Identify the blood parasite species.
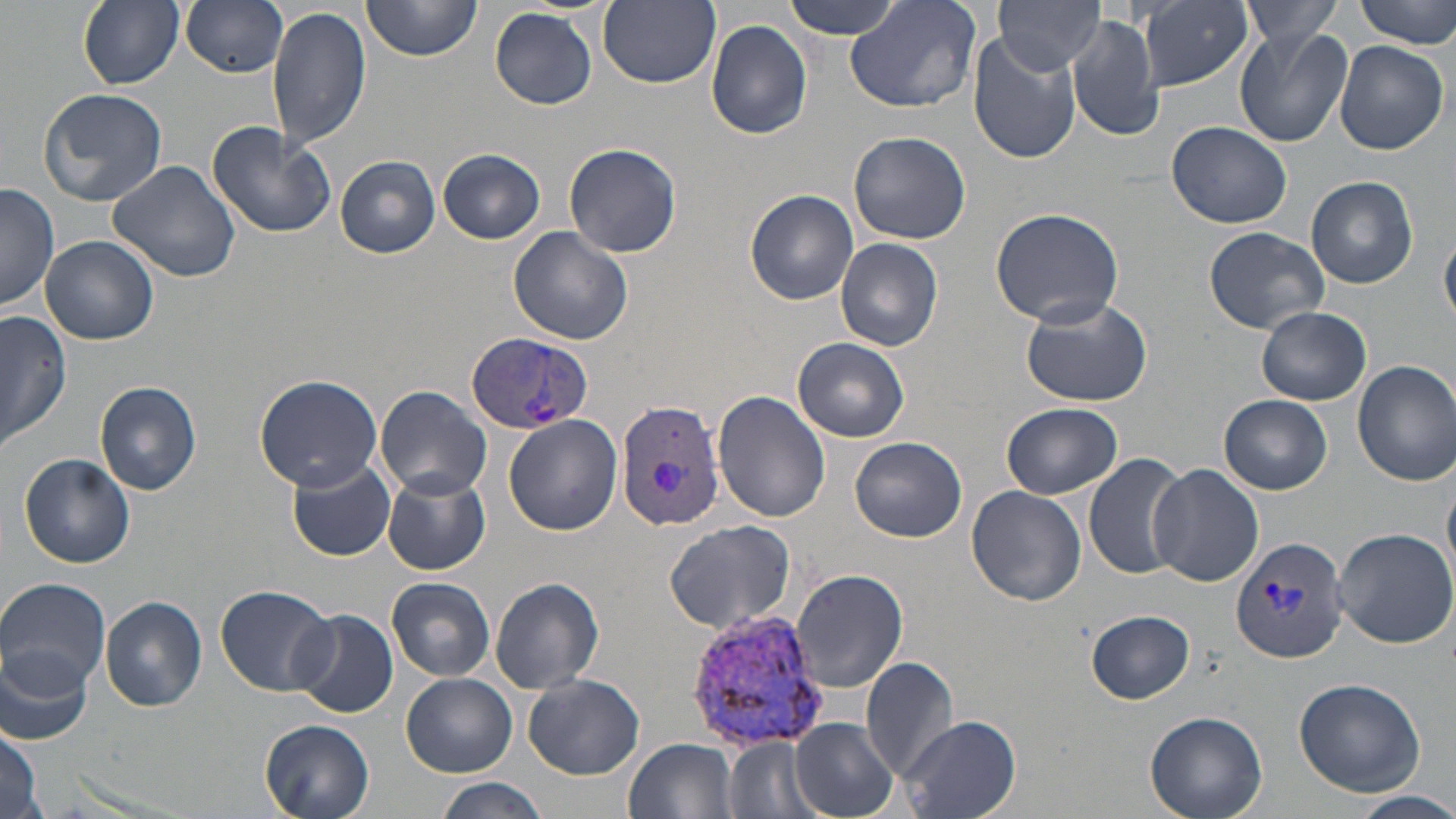

Plasmodium vivax.

Approximate bounding boxes as [x1, y1, x2, y2] in pixels. Plasmodium vivax-infected red blood cell locations: [466, 334, 594, 431], [615, 397, 727, 534], [1232, 538, 1351, 661], [682, 609, 832, 755]. Uninfected red blood cell locations: [78, 0, 184, 90], [181, 0, 290, 77], [361, 0, 480, 60], [783, 0, 907, 40], [844, 0, 982, 115], [1139, 0, 1252, 92], [1239, 0, 1344, 49], [1354, 0, 1456, 47], [599, 1, 720, 88], [992, 1, 1104, 73], [266, 5, 372, 149], [490, 7, 598, 109], [1068, 12, 1162, 140], [706, 20, 812, 140], [1234, 26, 1351, 147], [966, 33, 1082, 163], [1334, 39, 1448, 156], [37, 87, 168, 208], [206, 120, 337, 240], [1167, 122, 1295, 230], [848, 130, 970, 244], [563, 142, 683, 258], [439, 149, 544, 244], [336, 155, 440, 257], [107, 159, 240, 282], [1306, 176, 1418, 288], [1, 183, 59, 311], [75, 187, 226, 323], [746, 189, 859, 305], [989, 206, 1125, 327], [508, 227, 635, 348], [1203, 227, 1331, 334], [1441, 232, 1456, 327], [41, 236, 158, 345], [836, 237, 944, 352], [1018, 292, 1154, 406], [1256, 306, 1371, 406], [0, 310, 72, 454], [793, 339, 909, 441], [1353, 360, 1456, 485], [254, 373, 383, 491], [95, 381, 202, 494], [374, 385, 491, 500], [713, 390, 832, 523], [1219, 395, 1331, 494], [1001, 403, 1123, 500], [503, 414, 621, 536], [851, 437, 967, 542], [1083, 452, 1190, 583], [20, 453, 136, 568], [287, 457, 395, 561], [1148, 464, 1264, 587], [383, 472, 491, 575], [966, 485, 1087, 606], [666, 519, 797, 634], [1329, 526, 1456, 649], [790, 567, 908, 693], [387, 577, 496, 681], [490, 577, 604, 693], [0, 578, 111, 694], [215, 583, 337, 696], [99, 596, 207, 710], [1086, 610, 1196, 703], [291, 611, 398, 719], [1, 648, 95, 749], [861, 655, 960, 784], [403, 673, 516, 776], [523, 673, 644, 779], [1292, 678, 1425, 796], [1145, 711, 1267, 819], [900, 715, 1020, 819], [790, 718, 899, 819], [260, 719, 376, 819], [0, 729, 42, 819], [626, 736, 739, 819], [724, 736, 816, 819], [433, 777, 549, 819], [1343, 790, 1456, 819]. 1000x magnification. Light microscopy. May-Grünwald-Giemsa stain. One field of a larger specimen. Image is 1456×819 pixels. Thin blood smear.